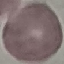 Result: no malaria parasites detected. Giemsa-stained preparation. Cell patch, automatically extracted from a larger field of view and resized to 64 × 64 pixels. Acquired by smartphone through the microscope eyepiece. Thin blood film.